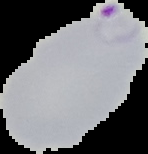
Summary:
  - Preparation: thin blood film
  - Image type: segmented cell region on a black background
  - Malaria status: parasitized
  - Image size: 148×154 pixels